Identify the parasite.
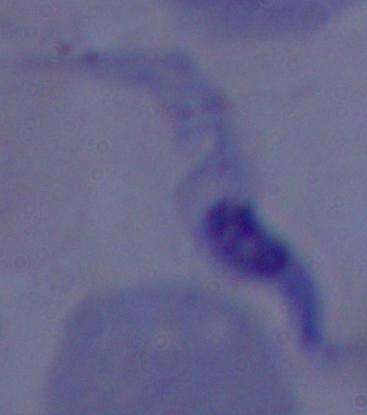

This is a trypanosome.

Summary:
  - Modality: photomicrograph
  - Magnification: 1000x